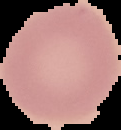
{
  "image_size": "121×130 pixels",
  "result": "no Plasmodium parasites detected",
  "preparation": "thin blood film",
  "image_type": "segmented cell region with the area outside set to black"
}